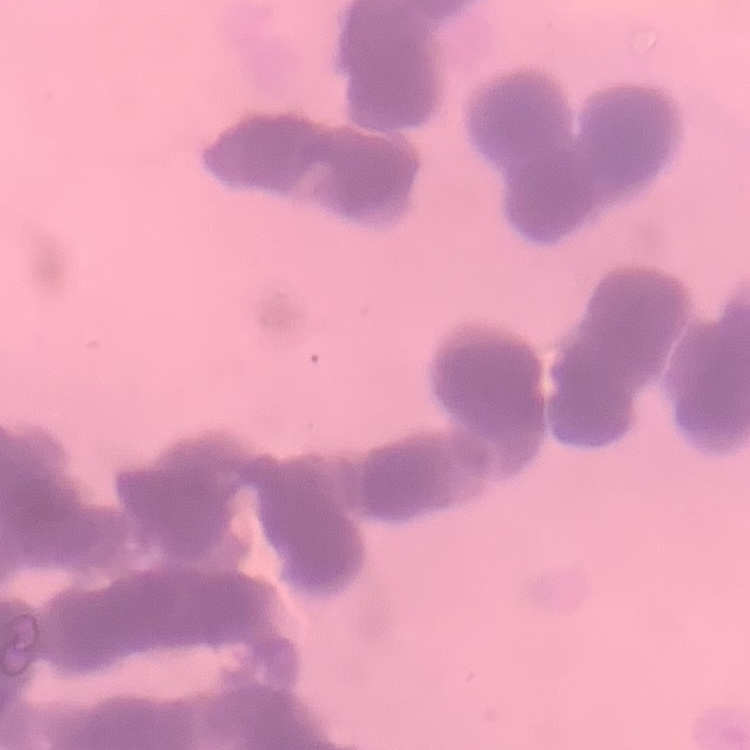

Summary:
  - Red blood cell morphology: rouleaux formation
  - Preparation: thin blood film
  - Stain: Field's or Giemsa
  - Image type: square crop of a larger photomicrograph